Point out each leukocyte.
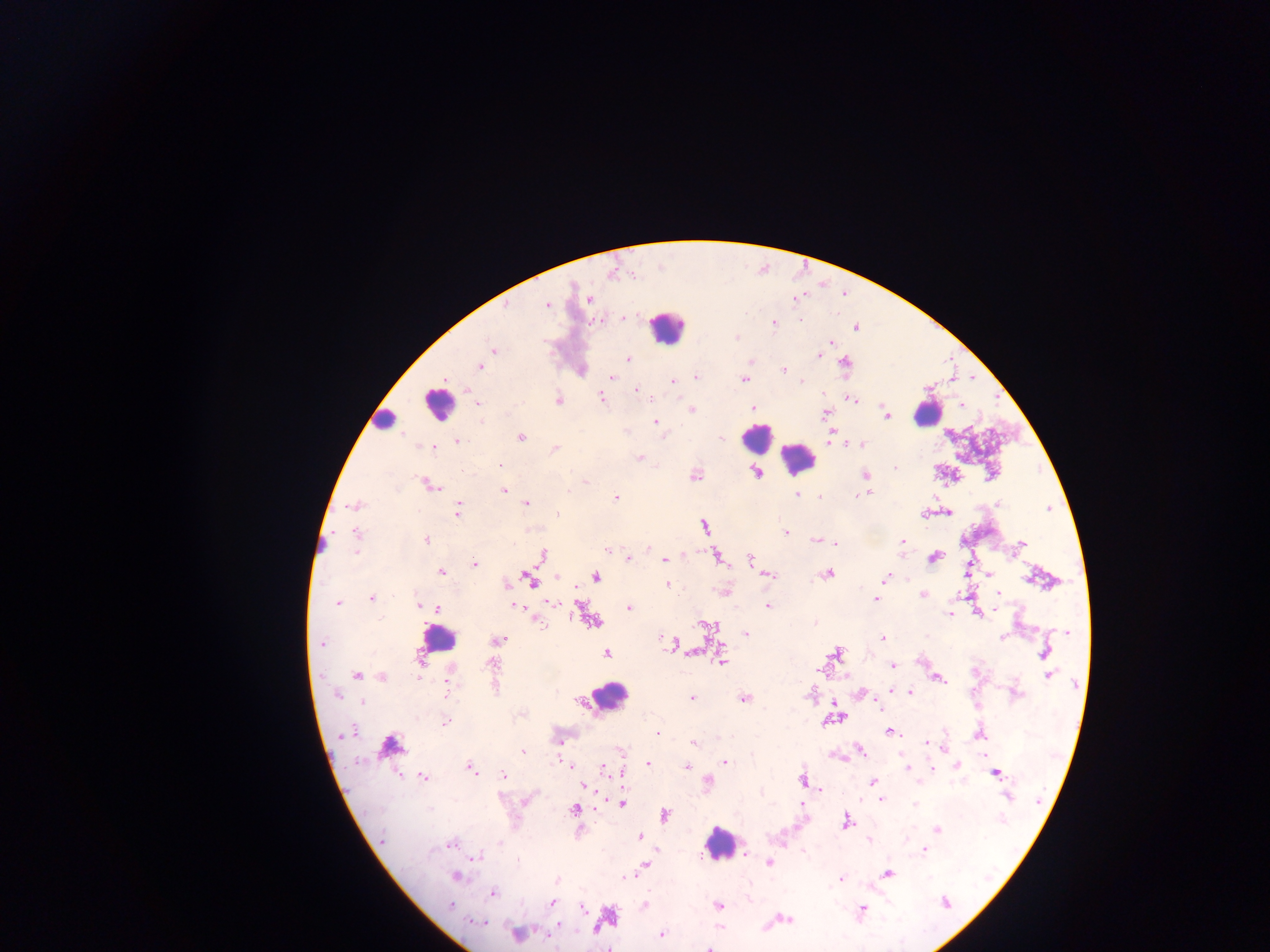

Approximate centers as x y in pixels.
Leukocytes: 667 328; 438 404; 928 412; 385 420; 756 438; 799 458; 607 696; 389 746; 718 844; 608 915.
One object is labeled both Plasmodium parasite and leukocyte by the source: 439 639.

Plasmodium parasite locations: 589 300; 548 304; 506 305; 623 318; 599 320; 799 320; 774 323; 856 327; 736 338; 831 342; 493 349; 819 356; 627 359; 750 362; 844 363; 479 366; 783 370; 611 377; 696 377; 743 379; 672 381; 801 381; 636 389; 822 394; 602 397; 851 398; 559 400; 477 403; 961 405; 753 408; 690 410; 886 413; 824 415; 655 422; 521 437; 720 437; 457 441; 860 444; 433 447; 554 449; 639 458; 501 465; 896 468; 756 473; 695 475; 866 475; 585 483; 429 484; 568 490; 504 491; 869 494; 798 495; 858 495; 616 498; 821 498; 526 503; 998 503; 354 506; 458 510; 949 513; 557 514; 924 514; 704 527; 785 532; 356 533; 426 540; 815 540; 902 541; 836 544; 1022 544; 648 549; 607 550; 355 553; 542 556; 718 557; 935 557; 629 559; 751 559; 664 561; 474 564; 442 572; 827 574; 989 574; 769 575; 557 577; 596 577; 886 578; 531 580; 668 585; 998 592; 923 595; 372 598; 876 600; 338 603; 551 603; 418 605; 768 605; 515 606; 629 608; 438 609; 996 609; 949 615; 593 621; 540 625; 710 628; 1068 632; 745 634; 660 636; 882 637; 1003 637; 500 639; 322 643; 836 652; 1045 652; 689 653; 606 654; 722 661; 492 664; 892 665; 356 675; 382 676; 1049 676; 418 678; 939 680; 449 682; 448 691; 909 691; 1016 694; 337 696; 692 698; 744 699; 362 703; 879 706; 835 718; 445 722; 890 732; 657 733; 347 734; 979 735; 561 741; 927 742; 693 743; 523 749; 861 750; 985 756; 725 762; 648 764; 958 764; 571 766; 687 766; 470 767; 907 767; 603 769; 932 769; 996 773; 503 775; 424 777; 708 780; 803 780; 873 782; 585 787; 821 789; 1008 795; 880 799; 527 800; 621 803; 915 804; 574 810; 665 815; 847 821; 937 830; 640 837; 869 841; 501 842; 451 843; 923 850; 745 853; 477 857; 517 861; 769 863; 645 865; 888 873; 627 876; 456 877; 840 878; 556 880; 493 892; 552 903; 945 903; 645 905; 717 905; 450 906; 583 908; 861 909; 787 920; 478 922; 517 934; 662 935; 709 948. Thick blood smear. Collected in Ghana. Photographed through a microscope with a mobile-phone camera. One field of view. Image is 1270×952 pixels.